Report the malaria status of this cell.
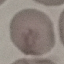

Uninfected.

{
  "image_type": "cell patch, automatically extracted from a larger field of view and resized to 64 × 64 pixels",
  "preparation": "thin smear",
  "stain": "Giemsa",
  "capture": "smartphone camera at the microscope eyepiece"
}